Identify the blood parasite species.
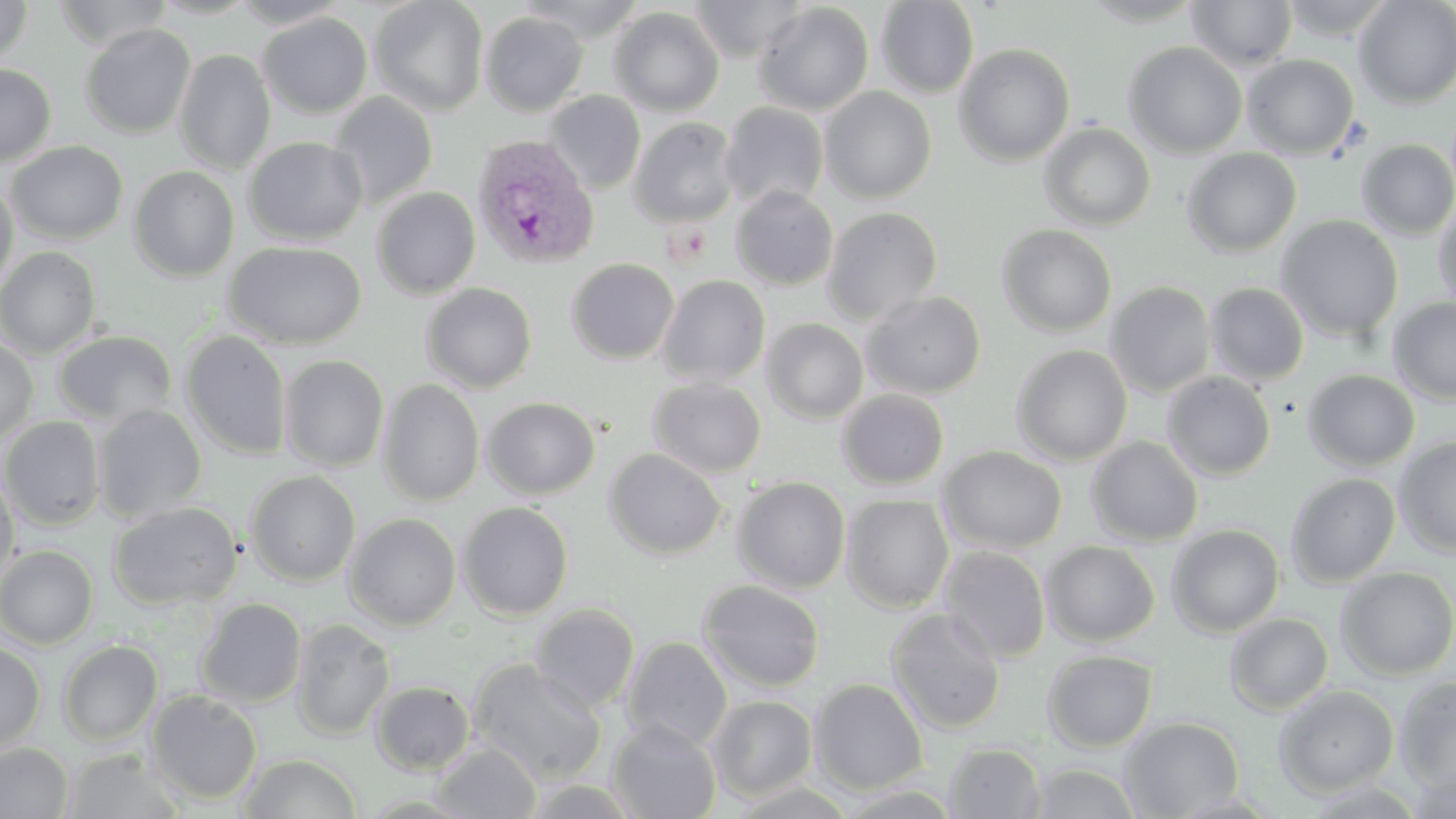
Plasmodium vivax.

Summary:
  - Coordinate format: approximate bounding boxes as (x1,y1)-(x2,y2) corner pairs in pixels
  - Plasmodium vivax-infected red blood cell locations: (471,135)-(599,269)
  - Platelet locations: (666,224)-(712,263)
  - Uninfected red blood cell locations: (0,0)-(33,64), (53,0)-(173,50), (150,0)-(260,20), (228,0)-(350,28), (369,0)-(489,116), (515,0)-(647,41), (689,0)-(810,62), (1078,0)-(1208,27), (1277,0)-(1401,41), (1354,0)-(1456,109), (875,1)-(979,97), (1186,1)-(1298,71), (752,3)-(874,116), (609,6)-(725,116), (481,11)-(588,116), (258,12)-(373,118), (80,23)-(196,139), (1123,41)-(1247,158), (954,43)-(1075,166), (173,49)-(275,175), (1241,54)-(1359,159), (0,64)-(56,167), (820,87)-(937,203), (544,90)-(646,194), (329,91)-(438,210), (719,102)-(829,211), (628,117)-(740,228), (1039,123)-(1156,231), (244,137)-(367,246), (1356,139)-(1456,239), (5,141)-(128,244), (1182,148)-(1302,257), (129,166)-(239,282), (0,177)-(18,297), (730,186)-(838,291), (371,187)-(481,299), (1432,199)-(1456,312), (822,207)-(943,325), (1276,215)-(1404,342), (997,224)-(1117,336), (224,240)-(366,349), (0,246)-(101,358), (566,258)-(679,365), (657,275)-(771,388), (1105,281)-(1216,398), (1204,282)-(1310,386), (421,283)-(537,393), (862,291)-(987,399), (1388,298)-(1456,405), (762,318)-(869,423), (53,330)-(177,427), (180,330)-(292,460), (0,338)-(38,447), (1011,344)-(1133,465), (278,354)-(389,472), (1303,369)-(1420,472), (1162,371)-(1276,480), (647,377)-(767,478), (378,378)-(485,506), (837,389)-(949,489), (482,396)-(600,499), (91,405)-(207,522), (1,416)-(106,531), (1086,436)-(1203,546), (1393,436)-(1456,557), (938,445)-(1067,554), (604,448)-(727,560), (0,469)-(20,589), (245,470)-(360,587), (1285,472)-(1401,588), (732,477)-(851,594), (841,494)-(954,612), (107,501)-(242,610), (457,502)-(573,620), (345,513)-(461,630), (1166,524)-(1285,636), (1041,541)-(1160,647), (0,545)-(98,649), (938,546)-(1052,662), (901,559)-(1039,708), (1335,567)-(1456,680), (697,579)-(825,693), (195,598)-(307,708), (529,603)-(640,712), (885,608)-(1007,734), (1224,613)-(1333,715), (290,617)-(395,741), (621,636)-(732,751), (0,640)-(46,756), (57,640)-(163,746), (1042,650)-(1158,752), (468,658)-(607,785), (1394,676)-(1456,791), (809,678)-(929,794), (371,681)-(475,775), (1273,685)-(1399,798), (145,690)-(263,805), (707,696)-(818,801), (1119,716)-(1244,818), (607,720)-(722,819), (0,742)-(73,818), (432,742)-(542,819), (944,742)-(1046,818), (60,748)-(187,819), (237,753)-(363,818), (1028,762)-(1143,818), (1407,765)-(1456,818), (520,779)-(643,818), (726,781)-(859,818)
  - Stain: May-Grünwald-Giemsa
  - Field of view: one of a larger specimen
  - Magnification: 1000x
  - Modality: light microscopy
  - Preparation: thin blood smear
  - Image size: 1456×819 pixels